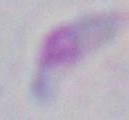 1000x magnification. Photomicrograph. Toxoplasma gondii is shown.